Classify this cell by malaria status.
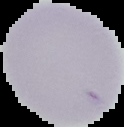
It is uninfected.

Summary:
  - Preparation: thin blood film
  - Image type: segmented cell region on a black background
  - Image size: 124×127 pixels